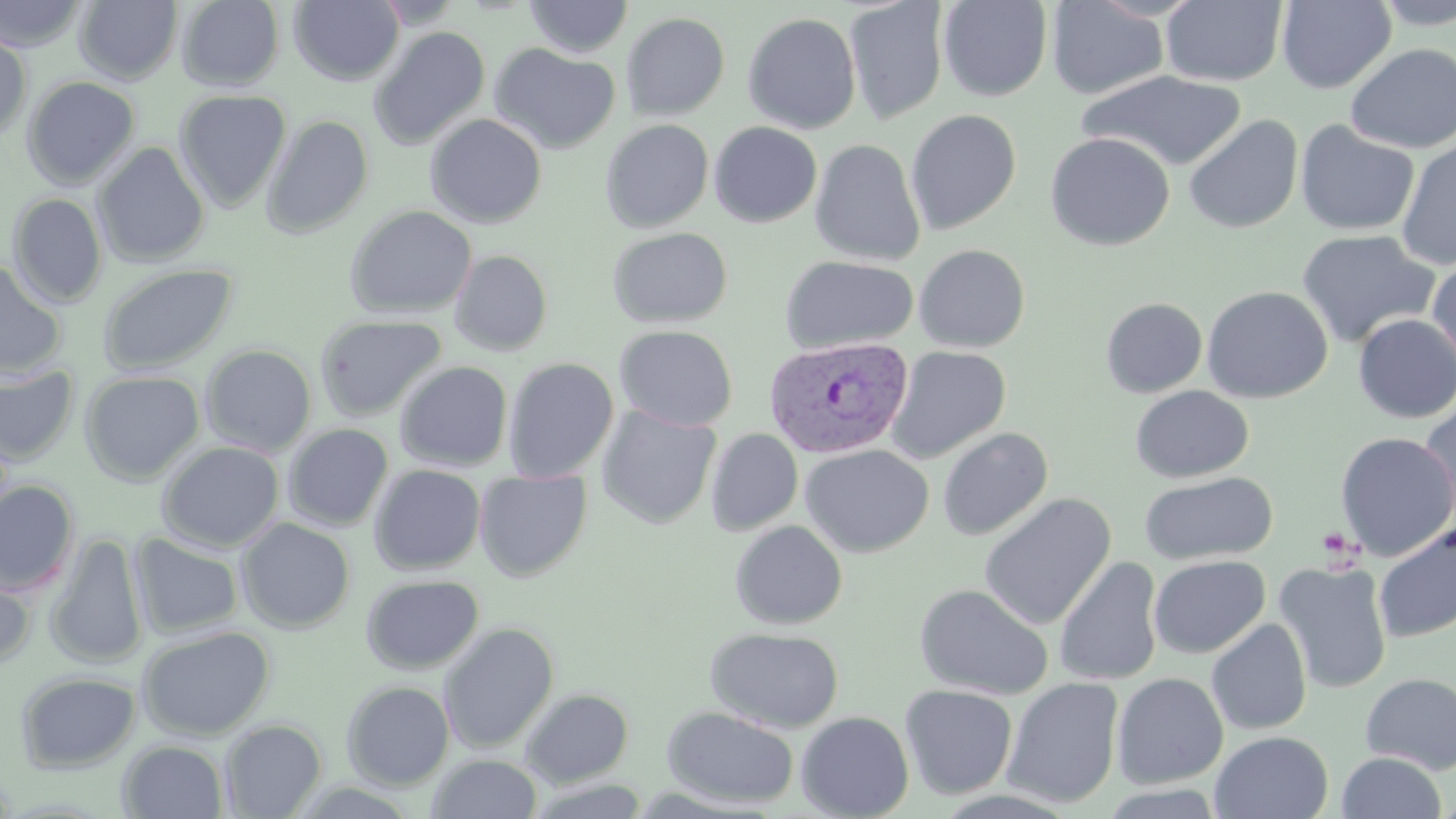

Summary:
  - Coordinate format: approximate bounding boxes as (x1,y1)-(x2,y2) corner pairs in pixels
  - Uninfected red blood cell locations: (0,0)-(90,52), (176,0)-(285,91), (289,0)-(404,86), (370,0)-(466,28), (938,0)-(1052,102), (1276,0)-(1396,93), (74,1)-(182,85), (523,1)-(634,58), (844,1)-(950,124), (1047,1)-(1169,99), (1160,1)-(1288,87), (1373,1)-(1456,30), (621,12)-(730,121), (742,12)-(862,135), (369,26)-(490,150), (0,29)-(32,142), (488,43)-(621,155), (1345,43)-(1456,154), (1077,70)-(1248,172), (21,75)-(141,190), (173,89)-(292,212), (905,109)-(1021,234), (425,113)-(547,229), (260,114)-(374,239), (1183,114)-(1303,234), (600,119)-(714,233), (1295,120)-(1420,237), (709,122)-(822,227), (1044,132)-(1175,251), (1396,138)-(1456,271), (810,139)-(926,266), (92,142)-(210,268), (7,193)-(107,307), (344,204)-(476,321), (606,227)-(733,329), (1296,228)-(1440,349), (914,244)-(1030,353), (449,249)-(553,357), (780,255)-(919,354), (1427,259)-(1456,382), (0,261)-(67,379), (98,262)-(238,376), (1201,285)-(1333,403), (1100,297)-(1207,398), (1353,314)-(1456,423), (315,315)-(447,422), (614,324)-(738,431), (200,344)-(317,456), (885,345)-(1011,463), (503,358)-(618,482), (394,360)-(513,472), (0,363)-(80,466), (79,369)-(205,485), (1130,385)-(1254,483), (1419,401)-(1456,529), (595,405)-(721,529), (282,423)-(393,531), (938,427)-(1053,541), (705,428)-(803,536), (1335,432)-(1456,562), (156,441)-(284,552), (799,443)-(934,558), (369,464)-(485,575), (474,470)-(592,582), (1139,470)-(1278,566), (0,480)-(80,597), (979,492)-(1116,631), (236,517)-(355,634), (729,520)-(848,630), (1373,522)-(1456,644), (46,532)-(148,669), (128,532)-(244,639), (1148,555)-(1270,658), (1054,556)-(1164,686), (1274,561)-(1393,694), (0,567)-(36,671), (361,574)-(483,674), (914,583)-(1054,700), (1206,618)-(1312,735), (438,622)-(559,753), (137,625)-(276,740), (705,626)-(844,733), (16,671)-(141,773), (1111,672)-(1229,789), (1360,672)-(1456,775), (1001,677)-(1124,808), (341,680)-(455,790), (900,684)-(1018,799), (520,687)-(634,787), (661,706)-(800,809), (796,711)-(914,819), (219,719)-(327,818), (1210,731)-(1334,819), (118,740)-(228,819), (1336,751)-(1448,818), (427,753)-(542,818), (523,777)-(652,818)
  - Platelet locations: (1317,528)-(1358,562)
  - Plasmodium vivax-infected red blood cell locations: (763,335)-(914,459)
  - Slide-level diagnosis: Plasmodium vivax
  - Image size: 1456×819 pixels
  - Stain: May-Grünwald-Giemsa
  - Preparation: thin blood film
  - Modality: light microscopy
  - Magnification: 1000x
  - Field of view: single